Locate every Plasmodium parasite.
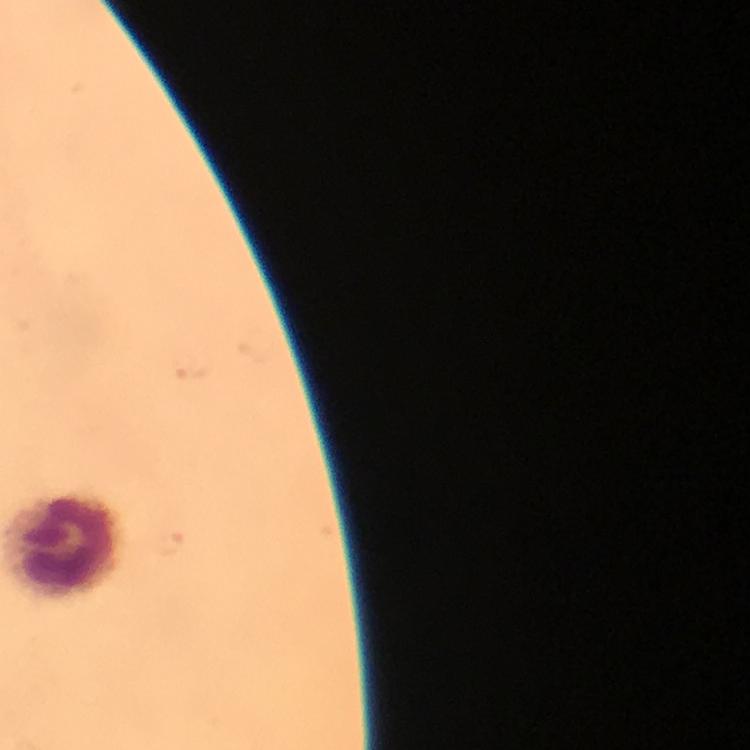
Approximate centers as {x, y} in pixels.
Plasmodium parasites: {184, 367}, {171, 544}.

Summary:
  - Leukocyte locations: {64, 545}
  - Cropped from: one field of view
  - Magnification: 100x
  - Capture: smartphone mounted on the microscope
  - Immersion oil: used
  - Stain: Giemsa
  - Image size: 750×750 pixels
  - Context: from a diagnostic examination for malaria
  - Preparation: thick blood smear